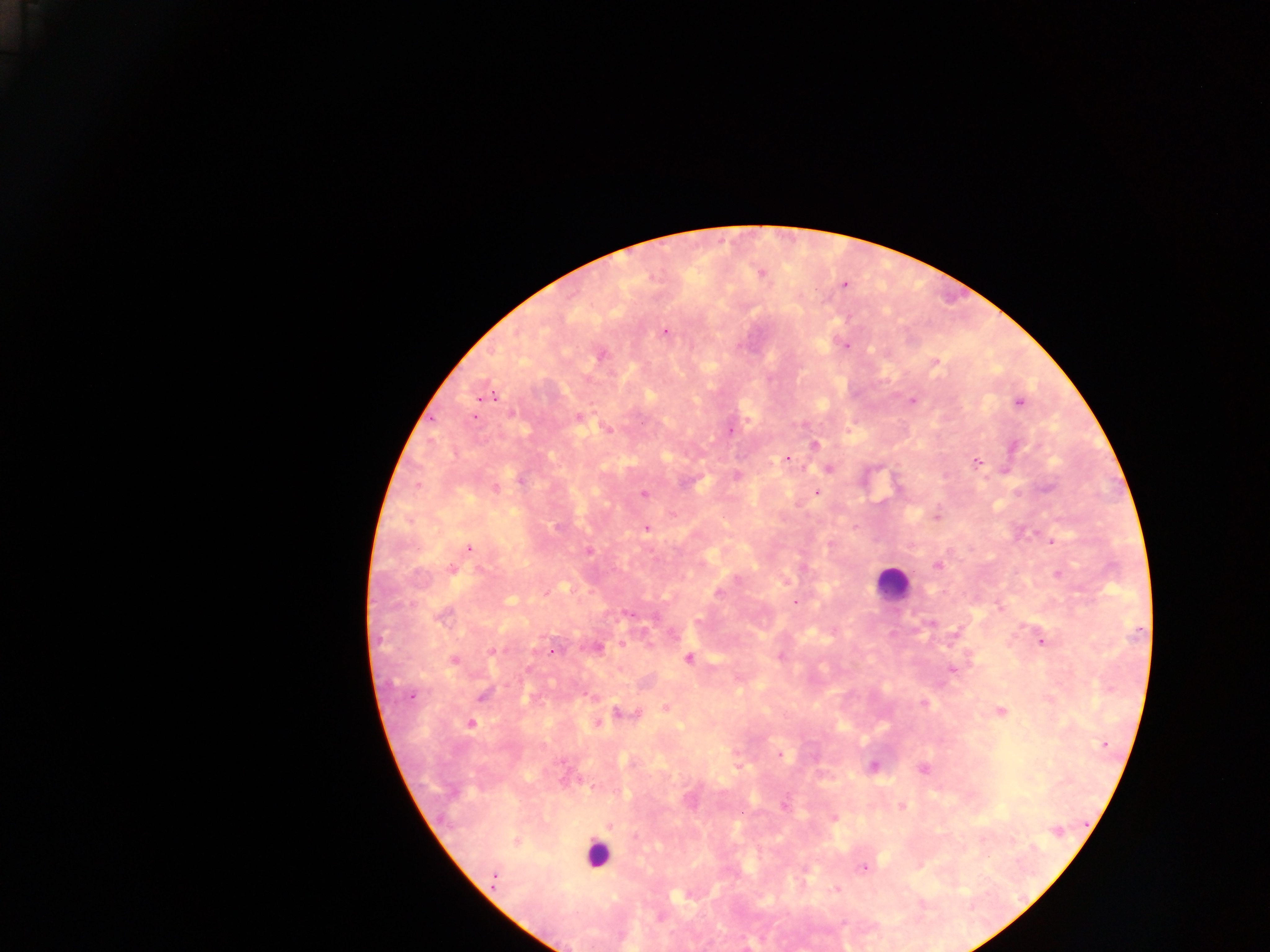 Approximate centers as {x, y} in pixels. Leukocyte locations: {893, 583}, {596, 854}. Plasmodium parasite locations: {760, 273}, {844, 284}, {665, 332}, {845, 346}, {600, 355}, {935, 363}, {486, 394}, {912, 401}, {1019, 403}, {511, 413}, {474, 418}, {578, 418}, {642, 422}, {607, 429}, {730, 430}, {814, 444}, {1014, 446}, {787, 459}, {977, 462}, {829, 469}, {736, 476}, {521, 480}, {495, 489}, {816, 492}, {643, 494}, {936, 516}, {557, 527}, {646, 528}, {1052, 541}, {469, 547}, {589, 551}, {938, 566}, {452, 569}, {1058, 574}, {718, 594}, {795, 603}, {1000, 607}, {627, 613}, {442, 616}, {931, 624}, {1043, 642}, {599, 648}, {553, 650}, {493, 651}, {688, 658}, {453, 660}, {952, 669}, {410, 696}, {482, 696}, {922, 703}, {666, 707}, {1001, 711}, {625, 714}, {597, 723}, {471, 724}, {1105, 744}, {779, 754}, {815, 757}, {873, 766}, {923, 768}, {785, 806}, {902, 807}, {834, 818}, {610, 826}, {1057, 831}, {516, 841}, {863, 868}, {494, 878}, {837, 889}. Image is 1270×952 pixels. Collected in Ghana. One field of view. Mobile-phone photograph taken through the microscope. Thick blood smear.